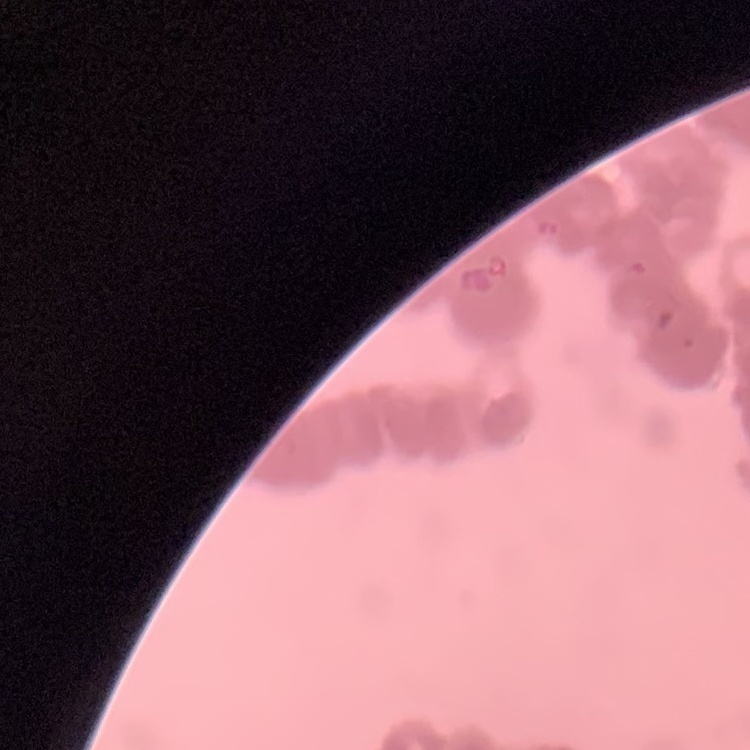 The erythrocytes exhibit rouleaux formation. Thin blood smear. One tile cut from a larger photomicrograph. Stained with either Field's or Giemsa.